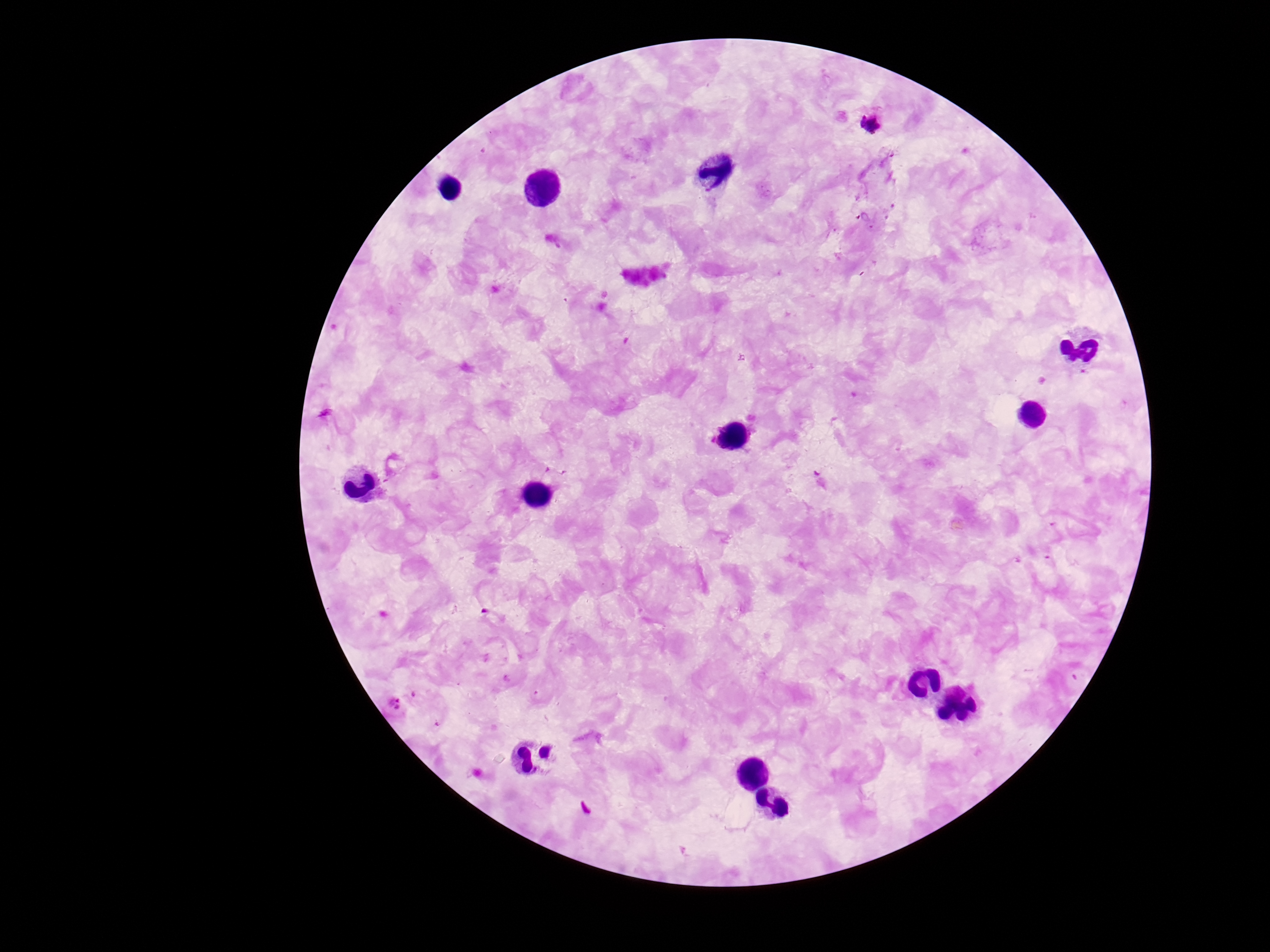
image_size: 1270×952 pixels
plasmodium_parasite_locations: 'approximate centers as [x, y] in pixels: [872, 123], [395, 705]'
stain: Giemsa
patient_malaria_status: positive
magnification: 100x
preparation: thick blood smear
capture: smartphone camera through the microscope eyepiece
field_of_view: one from this slide